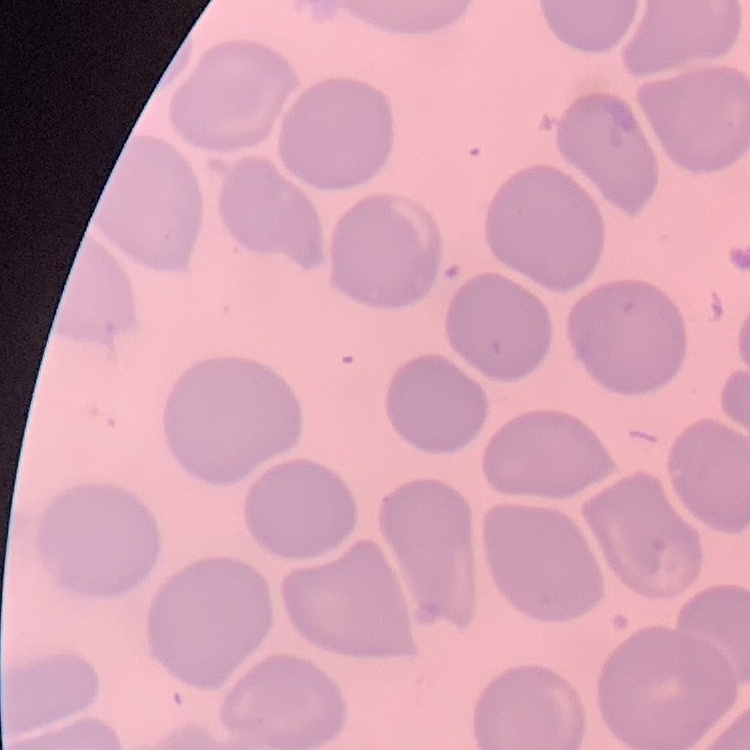
{
  "red_blood_cell_morphology": "no rouleaux formation",
  "stain": "Field's or Giemsa",
  "image_type": "square crop of a larger photomicrograph",
  "preparation": "thin peripheral smear"
}